Give the position of every malaria parasite.
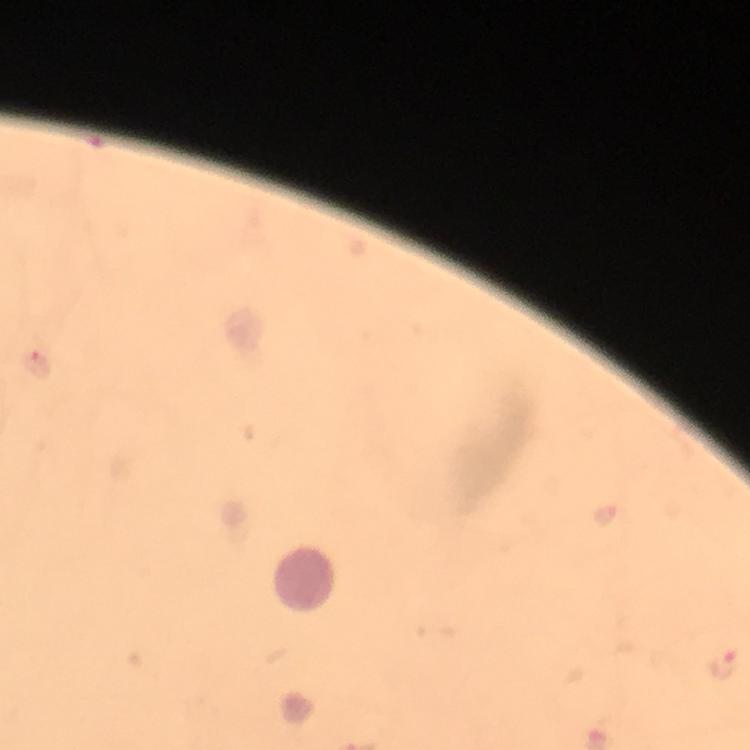
Approximate object centers, in pixels from the top-left corner.
Malaria parasites: (x=37, y=364), (x=723, y=663).

Thick blood smear. Photographed through the microscope with a smartphone camera. At 100x magnification. A crop from one field of view. Giemsa-stained preparation. Image is 750×750 pixels. From a diagnostic examination for malaria. Immersion oil was used.